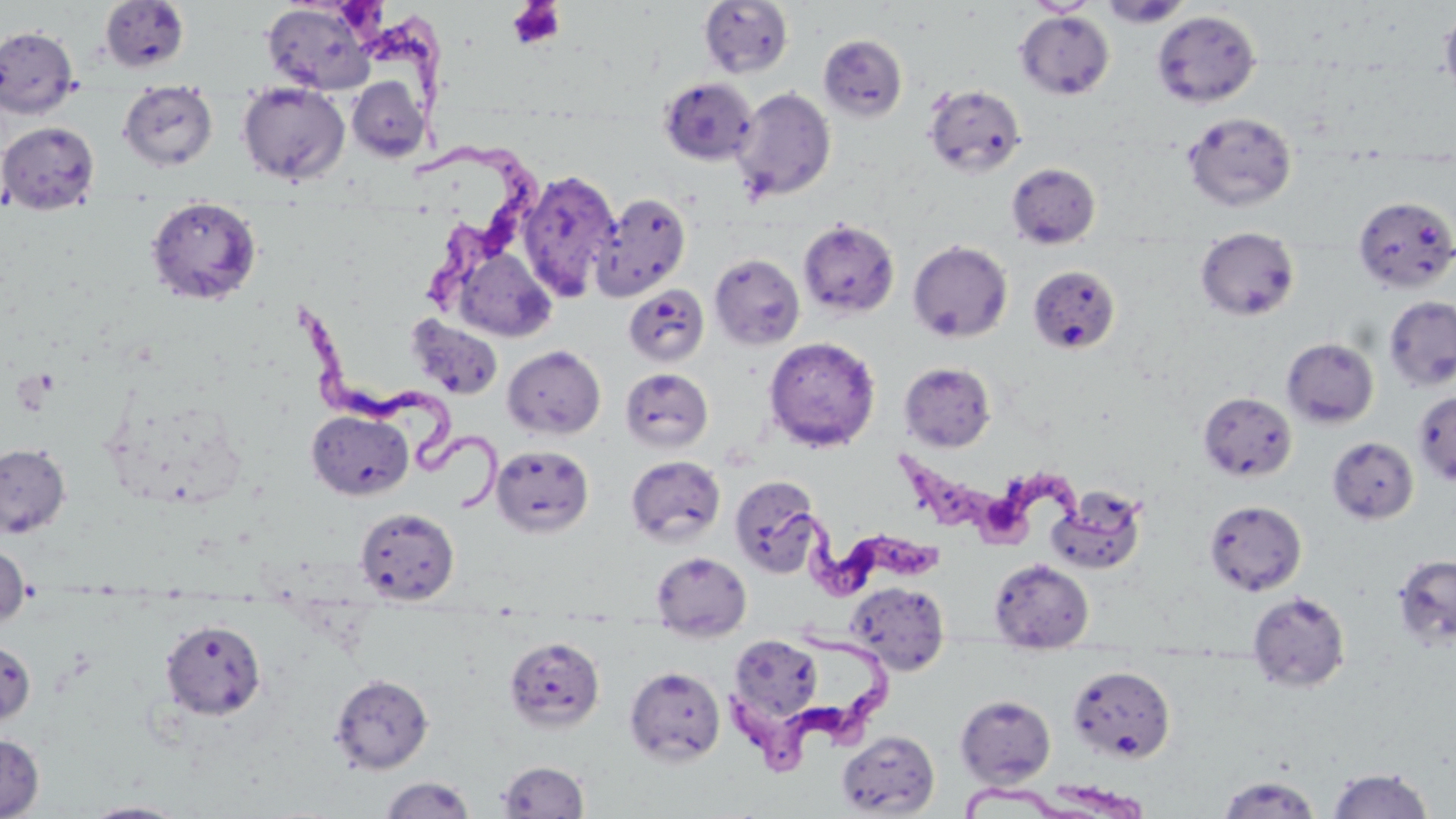
Summary:
  - Coordinate format: approximate bounding boxes as named x1/y1/x2/y2 corners in pixels
  - Uninfected red blood cell locations: (x1=1098, y1=0, x2=1192, y2=28), (x1=99, y1=1, x2=190, y2=72), (x1=699, y1=1, x2=794, y2=78), (x1=1025, y1=1, x2=1098, y2=16), (x1=261, y1=2, x2=377, y2=96), (x1=1439, y1=6, x2=1456, y2=104), (x1=1152, y1=10, x2=1261, y2=107), (x1=1015, y1=11, x2=1115, y2=100), (x1=0, y1=26, x2=79, y2=119), (x1=818, y1=34, x2=908, y2=122), (x1=346, y1=76, x2=430, y2=162), (x1=659, y1=77, x2=757, y2=165), (x1=238, y1=82, x2=350, y2=185), (x1=118, y1=83, x2=218, y2=171), (x1=923, y1=84, x2=1026, y2=178), (x1=732, y1=87, x2=836, y2=202), (x1=1182, y1=111, x2=1297, y2=212), (x1=0, y1=121, x2=99, y2=214), (x1=1006, y1=162, x2=1101, y2=248), (x1=517, y1=168, x2=622, y2=302), (x1=591, y1=192, x2=690, y2=302), (x1=146, y1=196, x2=262, y2=305), (x1=1353, y1=196, x2=1456, y2=293), (x1=798, y1=218, x2=900, y2=318), (x1=1196, y1=227, x2=1300, y2=321), (x1=907, y1=239, x2=1013, y2=343), (x1=453, y1=246, x2=556, y2=342), (x1=709, y1=253, x2=805, y2=350), (x1=1028, y1=265, x2=1121, y2=355), (x1=623, y1=285, x2=710, y2=367), (x1=1384, y1=296, x2=1456, y2=392), (x1=407, y1=315, x2=504, y2=400), (x1=764, y1=336, x2=881, y2=452), (x1=1282, y1=337, x2=1379, y2=428), (x1=503, y1=345, x2=605, y2=439), (x1=899, y1=362, x2=996, y2=451), (x1=620, y1=368, x2=713, y2=452), (x1=1413, y1=390, x2=1456, y2=487), (x1=1198, y1=391, x2=1298, y2=482), (x1=307, y1=410, x2=413, y2=500), (x1=1327, y1=436, x2=1419, y2=524), (x1=0, y1=443, x2=71, y2=538), (x1=491, y1=444, x2=594, y2=537), (x1=626, y1=455, x2=726, y2=546), (x1=730, y1=476, x2=823, y2=577), (x1=1049, y1=487, x2=1148, y2=574), (x1=1204, y1=500, x2=1307, y2=596), (x1=355, y1=507, x2=459, y2=604), (x1=0, y1=540, x2=30, y2=629), (x1=651, y1=551, x2=752, y2=642), (x1=1392, y1=553, x2=1456, y2=650), (x1=989, y1=558, x2=1094, y2=652), (x1=846, y1=581, x2=950, y2=674), (x1=1248, y1=591, x2=1350, y2=692), (x1=160, y1=619, x2=267, y2=719), (x1=728, y1=634, x2=823, y2=727), (x1=504, y1=636, x2=605, y2=732), (x1=0, y1=637, x2=36, y2=727), (x1=1068, y1=665, x2=1176, y2=763), (x1=624, y1=666, x2=726, y2=766), (x1=330, y1=674, x2=434, y2=774), (x1=955, y1=695, x2=1056, y2=786), (x1=836, y1=730, x2=940, y2=816), (x1=0, y1=733, x2=43, y2=819), (x1=497, y1=761, x2=589, y2=817), (x1=1327, y1=767, x2=1434, y2=818), (x1=1216, y1=775, x2=1322, y2=818), (x1=380, y1=776, x2=475, y2=818), (x1=79, y1=801, x2=192, y2=818)
  - Platelet locations: (x1=507, y1=1, x2=566, y2=50)
  - Trypanosoma brucei locations: (x1=327, y1=0, x2=458, y2=104), (x1=412, y1=144, x2=548, y2=313), (x1=294, y1=306, x2=512, y2=521), (x1=901, y1=447, x2=1145, y2=549), (x1=761, y1=505, x2=952, y2=609), (x1=733, y1=627, x2=904, y2=773), (x1=960, y1=774, x2=1152, y2=819)
  - Slide-level diagnosis: Trypanosoma brucei
  - Magnification: 1000x
  - Field of view: single
  - Stain: May-Grünwald-Giemsa
  - Modality: light microscopy
  - Preparation: thin blood film
  - Image size: 1456×819 pixels